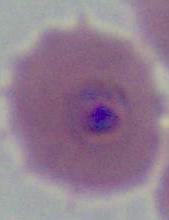
identification = Plasmodium
magnification = 400x or 1000x
modality = micrograph